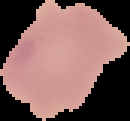

preparation: thin blood film
image_size: 130×121 pixels
result: no Plasmodium parasites seen
image_type: segmented cell region with the area outside set to black